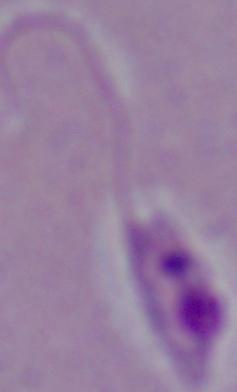

modality = photomicrograph
identification = Leishmania
magnification = 1000x